Locate malaria parasites and leukocytes.
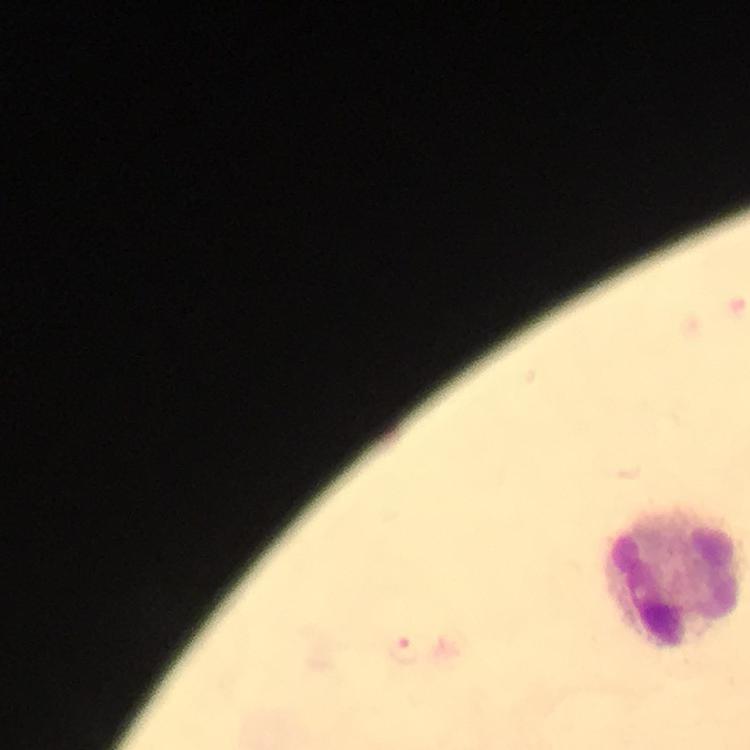
Approximate centers as [x, y] in pixels.
Malaria parasites: [404, 651].
Leukocytes: [675, 577].

Immersion oil was used. Photographed through the microscope with a smartphone camera. Thick blood smear. Image is 750×750 pixels. From a diagnostic examination for malaria. Cropped region of a single field of view. At 100x magnification. Giemsa stain.